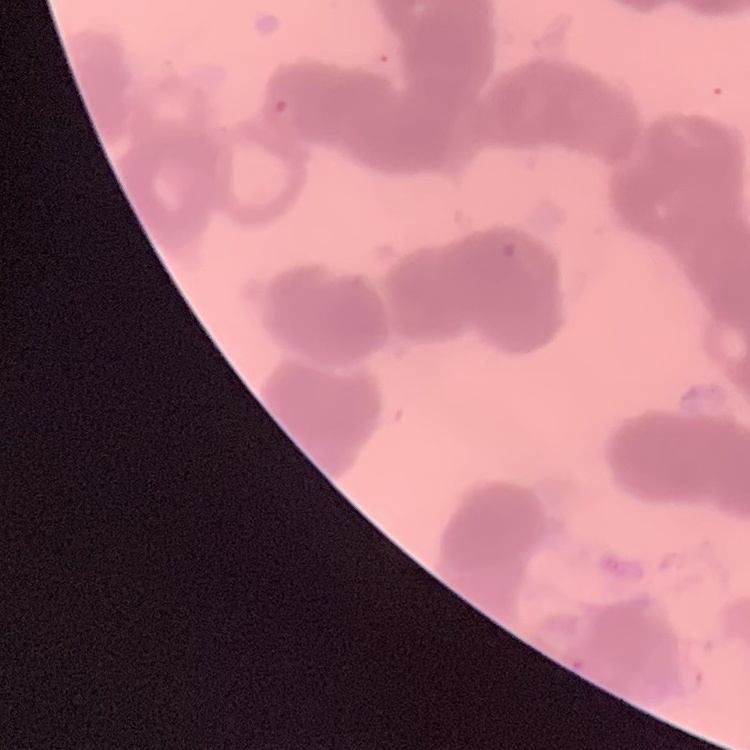 The erythrocytes show rouleaux formation. One tile cut from a larger photomicrograph. Stained with either Field's or Giemsa. Thin blood film.